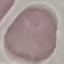

{
  "result": "no malaria parasites detected",
  "capture": "smartphone camera at the microscope eyepiece",
  "stain": "Giemsa",
  "preparation": "thin blood film",
  "image_type": "cell patch, automatically extracted from a larger field of view and resized to 64 × 64 pixels"
}